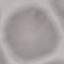

Malaria status: uninfected. Giemsa stain. Automatically extracted cell patch, resized to 64 × 64 pixels. Acquired by smartphone through the microscope eyepiece. Thin blood film.